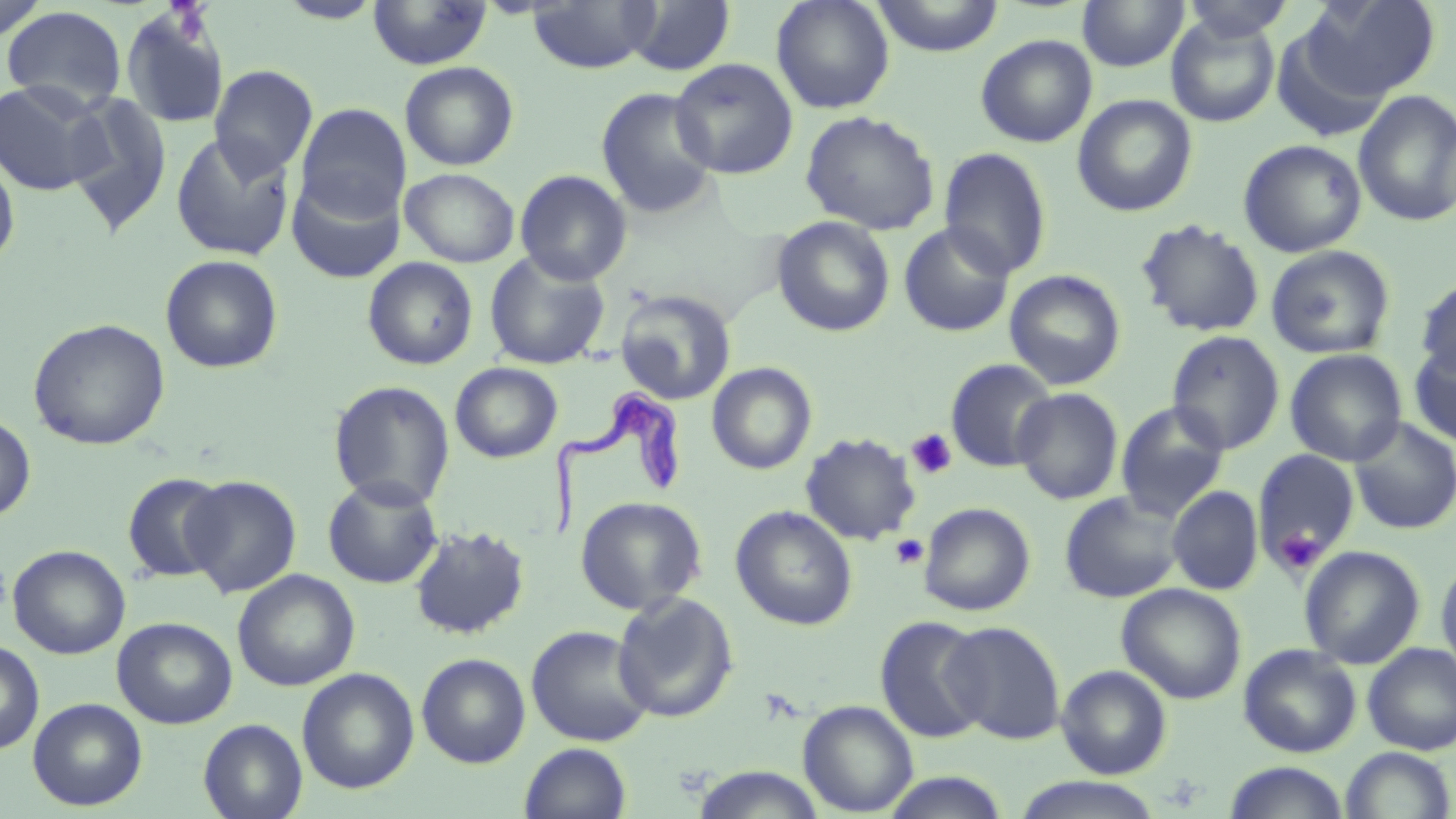

Summary:
  - Coordinate format: approximate bounding boxes as named x1/y1/x2/y2 corners in pixels
  - Uninfected red blood cell locations: (x1=275, y1=0, x2=386, y2=24), (x1=367, y1=0, x2=491, y2=70), (x1=527, y1=0, x2=660, y2=74), (x1=625, y1=0, x2=735, y2=76), (x1=771, y1=0, x2=895, y2=114), (x1=870, y1=0, x2=1004, y2=56), (x1=1077, y1=0, x2=1190, y2=72), (x1=1180, y1=0, x2=1295, y2=42), (x1=1301, y1=0, x2=1441, y2=101), (x1=0, y1=2, x2=50, y2=43), (x1=1, y1=5, x2=127, y2=113), (x1=121, y1=9, x2=230, y2=129), (x1=1166, y1=14, x2=1280, y2=127), (x1=975, y1=34, x2=1097, y2=147), (x1=670, y1=58, x2=799, y2=179), (x1=399, y1=61, x2=519, y2=170), (x1=209, y1=64, x2=318, y2=179), (x1=1, y1=80, x2=108, y2=195), (x1=595, y1=86, x2=720, y2=219), (x1=1353, y1=90, x2=1456, y2=228), (x1=65, y1=92, x2=173, y2=235), (x1=1072, y1=94, x2=1197, y2=216), (x1=295, y1=103, x2=411, y2=222), (x1=800, y1=110, x2=940, y2=234), (x1=170, y1=132, x2=296, y2=261), (x1=1238, y1=139, x2=1367, y2=258), (x1=938, y1=147, x2=1052, y2=280), (x1=0, y1=151, x2=20, y2=269), (x1=401, y1=168, x2=519, y2=267), (x1=515, y1=169, x2=632, y2=285), (x1=287, y1=170, x2=406, y2=284), (x1=771, y1=216, x2=895, y2=337), (x1=1136, y1=219, x2=1265, y2=338), (x1=898, y1=222, x2=1015, y2=338), (x1=1266, y1=245, x2=1396, y2=359), (x1=484, y1=250, x2=611, y2=370), (x1=160, y1=254, x2=284, y2=374), (x1=362, y1=257, x2=479, y2=370), (x1=1004, y1=270, x2=1126, y2=391), (x1=1415, y1=276, x2=1456, y2=381), (x1=614, y1=289, x2=736, y2=405), (x1=28, y1=318, x2=170, y2=451), (x1=1166, y1=330, x2=1285, y2=455), (x1=1408, y1=338, x2=1456, y2=448), (x1=1285, y1=348, x2=1408, y2=467), (x1=945, y1=358, x2=1057, y2=472), (x1=450, y1=362, x2=562, y2=463), (x1=706, y1=362, x2=817, y2=475), (x1=328, y1=380, x2=455, y2=509), (x1=1012, y1=388, x2=1124, y2=505), (x1=1115, y1=402, x2=1230, y2=521), (x1=0, y1=412, x2=36, y2=522), (x1=1348, y1=417, x2=1456, y2=535), (x1=800, y1=432, x2=921, y2=546), (x1=1252, y1=449, x2=1360, y2=574), (x1=121, y1=471, x2=231, y2=584), (x1=181, y1=475, x2=302, y2=598), (x1=322, y1=476, x2=444, y2=589), (x1=356, y1=485, x2=518, y2=607), (x1=1167, y1=486, x2=1264, y2=595), (x1=1059, y1=490, x2=1186, y2=603), (x1=574, y1=495, x2=707, y2=615), (x1=919, y1=502, x2=1036, y2=616), (x1=730, y1=505, x2=858, y2=631), (x1=409, y1=524, x2=530, y2=640), (x1=8, y1=544, x2=130, y2=659), (x1=1299, y1=545, x2=1425, y2=669), (x1=1436, y1=555, x2=1456, y2=682), (x1=232, y1=570, x2=360, y2=691), (x1=1117, y1=582, x2=1247, y2=704), (x1=611, y1=591, x2=739, y2=723), (x1=875, y1=615, x2=991, y2=744), (x1=112, y1=616, x2=238, y2=729), (x1=941, y1=621, x2=1066, y2=745), (x1=525, y1=625, x2=656, y2=747), (x1=0, y1=640, x2=45, y2=754), (x1=1362, y1=643, x2=1456, y2=756), (x1=1238, y1=644, x2=1362, y2=758), (x1=416, y1=652, x2=531, y2=768), (x1=1056, y1=664, x2=1172, y2=779), (x1=297, y1=667, x2=420, y2=794), (x1=28, y1=697, x2=147, y2=811), (x1=798, y1=700, x2=919, y2=816), (x1=198, y1=718, x2=308, y2=819), (x1=519, y1=742, x2=633, y2=819), (x1=1339, y1=746, x2=1455, y2=819), (x1=1222, y1=761, x2=1351, y2=819), (x1=689, y1=766, x2=827, y2=819), (x1=878, y1=772, x2=1014, y2=819), (x1=1011, y1=776, x2=1165, y2=818)
  - Trypanosoma brucei locations: (x1=552, y1=383, x2=689, y2=541)
  - Platelet locations: (x1=906, y1=428, x2=959, y2=479), (x1=1273, y1=528, x2=1324, y2=575), (x1=890, y1=534, x2=929, y2=568)
  - Slide-level diagnosis: Trypanosoma brucei
  - Image size: 1456×819 pixels
  - Field of view: single
  - Stain: May-Grünwald-Giemsa
  - Preparation: thin blood film
  - Magnification: 1000x
  - Modality: optical microscopy